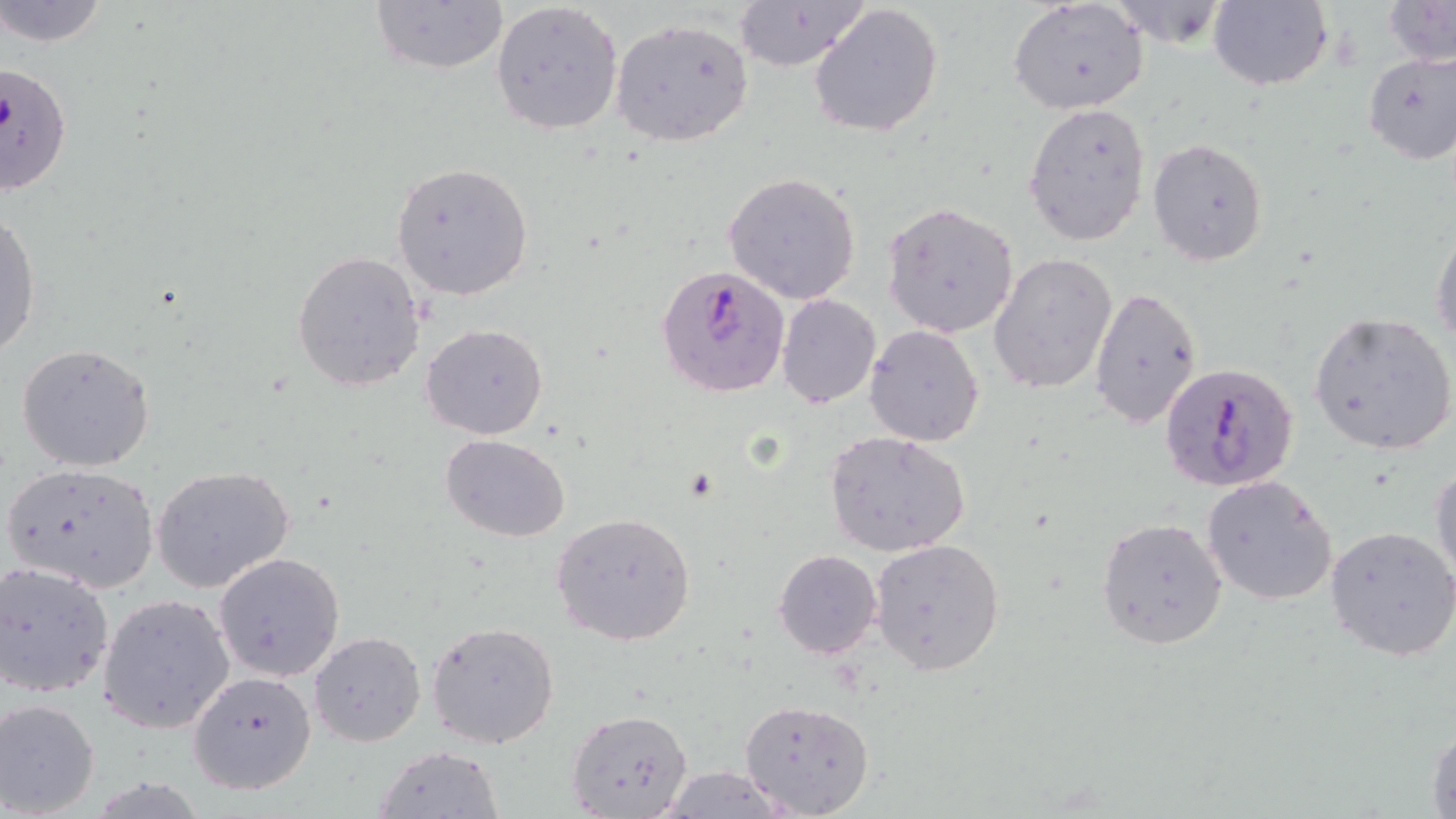
slide_level_diagnosis: Plasmodium falciparum
modality: light microscopy
magnification: 1000x
stain: May-Grünwald-Giemsa
plasmodium_falciparum_infected_red_blood_cell_locations: 'approximate bounding boxes as [x1, y1, x2, y2] in pixels: [1, 60, 73, 198], [655, 264, 790, 399], [1158, 360, 1300, 494]'
uninfected_red_blood_cell_locations: 'approximate bounding boxes as [x1, y1, x2, y2] in pixels: [0, 0, 110, 49], [369, 0, 508, 74], [1009, 0, 1149, 116], [1207, 0, 1333, 92], [1381, 0, 1456, 68], [732, 1, 870, 73], [808, 1, 945, 139], [491, 2, 624, 136], [609, 18, 755, 149], [1359, 48, 1456, 164], [1021, 102, 1152, 247], [1147, 137, 1269, 266], [391, 161, 534, 302], [723, 171, 862, 303], [883, 203, 1019, 339], [0, 210, 41, 359], [1431, 227, 1456, 349], [292, 251, 426, 393], [988, 252, 1116, 396], [1088, 286, 1203, 429], [776, 293, 882, 409], [1307, 312, 1456, 456], [421, 322, 548, 440], [864, 324, 985, 447], [15, 344, 155, 471], [823, 430, 972, 558], [440, 433, 570, 541], [1431, 457, 1456, 586], [3, 462, 161, 595], [150, 464, 296, 593], [1201, 475, 1340, 607], [554, 511, 696, 645], [1097, 517, 1228, 650], [1325, 525, 1456, 663], [870, 538, 1006, 675], [772, 548, 882, 660], [212, 551, 346, 682], [1, 561, 115, 698], [99, 594, 234, 734], [426, 621, 561, 748], [309, 631, 426, 747], [187, 670, 318, 796], [0, 698, 102, 817], [740, 699, 875, 817], [567, 708, 692, 819], [1427, 719, 1456, 819], [371, 744, 506, 819], [655, 766, 797, 819]'
field_of_view: one of a larger specimen
preparation: thin blood smear
image_size: 1456×819 pixels